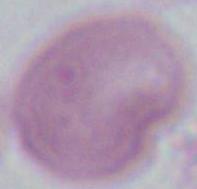

Summary:
  - Magnification: 1000x
  - Identification: erythrocyte
  - Modality: micrograph